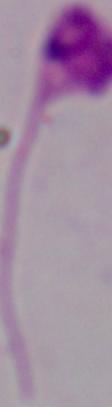
Captured at 1000x magnification. Photomicrograph. A Leishmania parasite is seen.